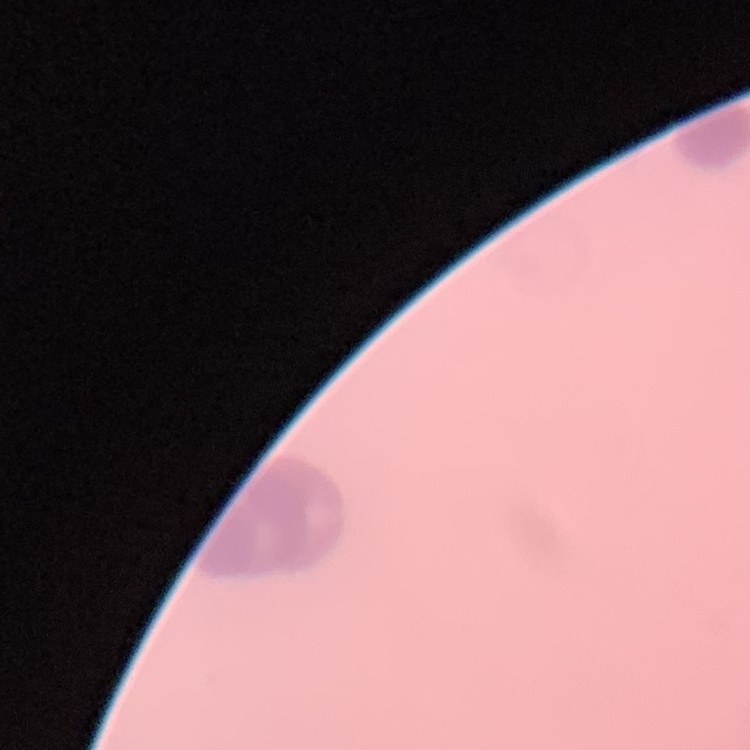

red blood cell morphology = rouleaux formation
preparation = thin peripheral smear
image type = square crop of a larger photomicrograph
stain = Field's or Giemsa